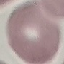
{
  "result": "no malaria parasites detected",
  "image_type": "automatically extracted cell patch, resized to 64 × 64 pixels",
  "preparation": "thin smear",
  "stain": "Giemsa",
  "capture": "smartphone through the microscope eyepiece"
}